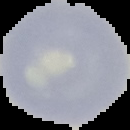

image size = 130×130 pixels
preparation = thin blood smear
image type = cell region segmented out of the field of view; surrounding area masked to black
malaria status = uninfected